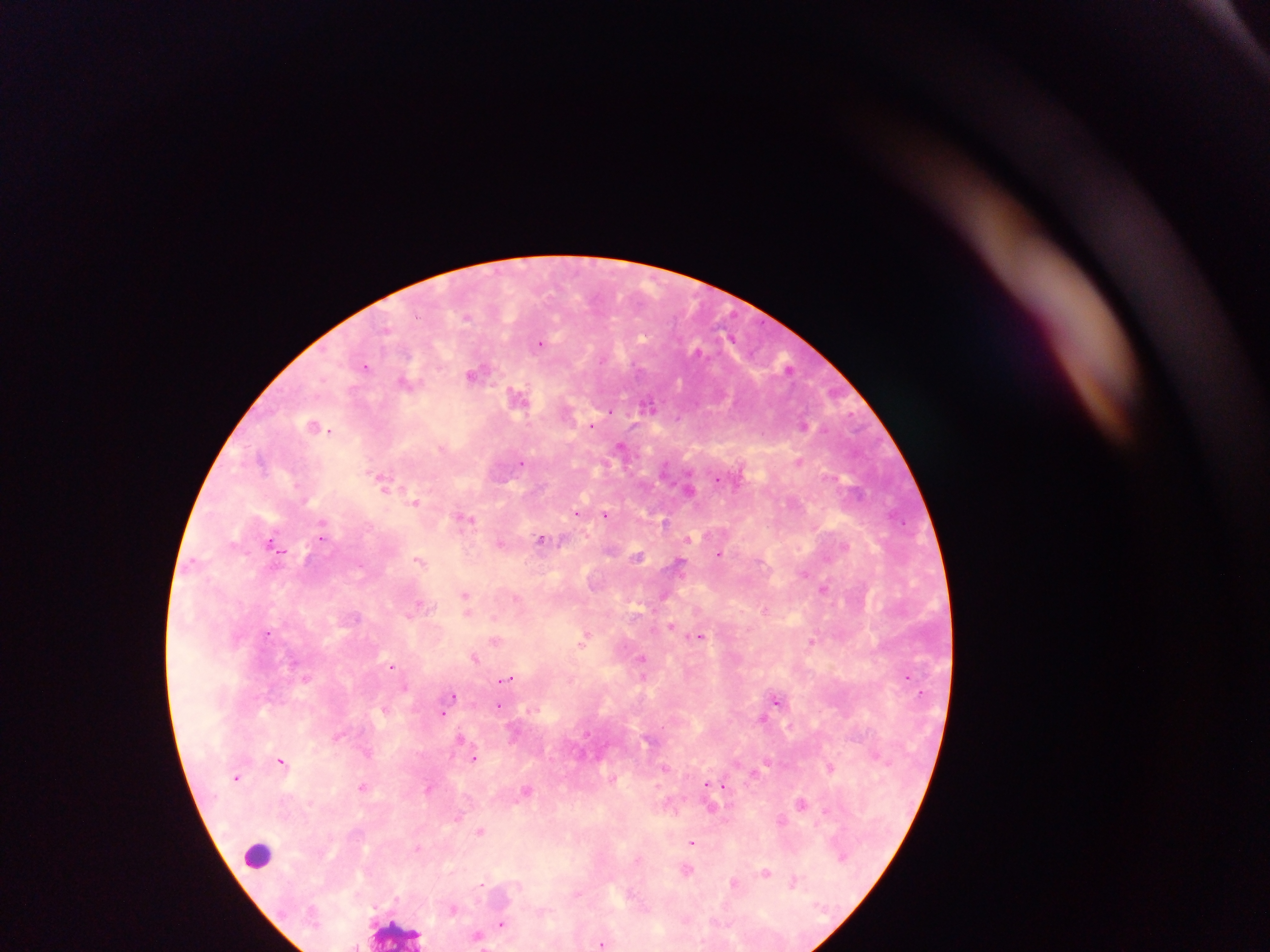 Approximate centers as {x, y} in pixels. Leukocyte locations: {258, 854}, {398, 932}. Malaria parasite locations: {540, 343}, {699, 352}, {366, 365}, {788, 369}, {475, 373}, {406, 382}, {520, 397}, {650, 405}, {804, 424}, {316, 425}, {592, 425}, {622, 447}, {799, 461}, {521, 462}, {382, 481}, {689, 489}, {416, 501}, {578, 512}, {606, 515}, {465, 517}, {665, 522}, {323, 534}, {689, 538}, {542, 539}, {274, 543}, {501, 543}, {721, 553}, {638, 556}, {420, 561}, {680, 564}, {804, 571}, {823, 588}, {466, 596}, {664, 596}, {419, 603}, {767, 609}, {468, 613}, {671, 625}, {268, 631}, {698, 636}, {585, 639}, {496, 640}, {812, 641}, {475, 657}, {642, 659}, {392, 666}, {908, 675}, {307, 677}, {507, 678}, {405, 687}, {454, 695}, {777, 699}, {498, 705}, {385, 708}, {442, 713}, {764, 718}, {791, 727}, {338, 734}, {462, 738}, {369, 751}, {475, 758}, {282, 760}, {767, 763}, {831, 766}, {666, 767}, {236, 777}, {614, 778}, {708, 783}, {363, 786}, {725, 787}, {428, 788}, {528, 789}, {802, 803}, {712, 808}, {459, 816}, {481, 830}, {693, 843}, {418, 847}, {1263, 859}, {687, 870}, {767, 871}, {795, 880}, {736, 882}, {481, 884}, {453, 908}, {502, 923}, {479, 934}, {603, 942}. Single field of view. Mobile-phone photograph taken through the microscope. Image is 1270×952 pixels. Thick blood smear. Collected in Ghana.